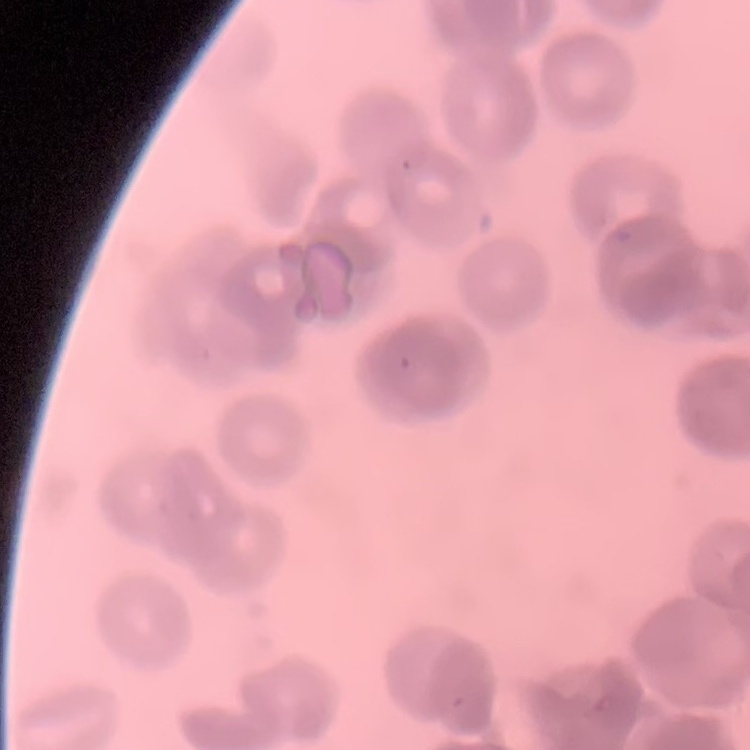
erythrocyte morphology = rouleaux formation
image type = square crop of a larger photomicrograph
preparation = thin peripheral smear
stain = Field's or Giemsa